Find the red blood cells and label each as P. falciparum-infected, uninfected, or of indeterminate infection status.
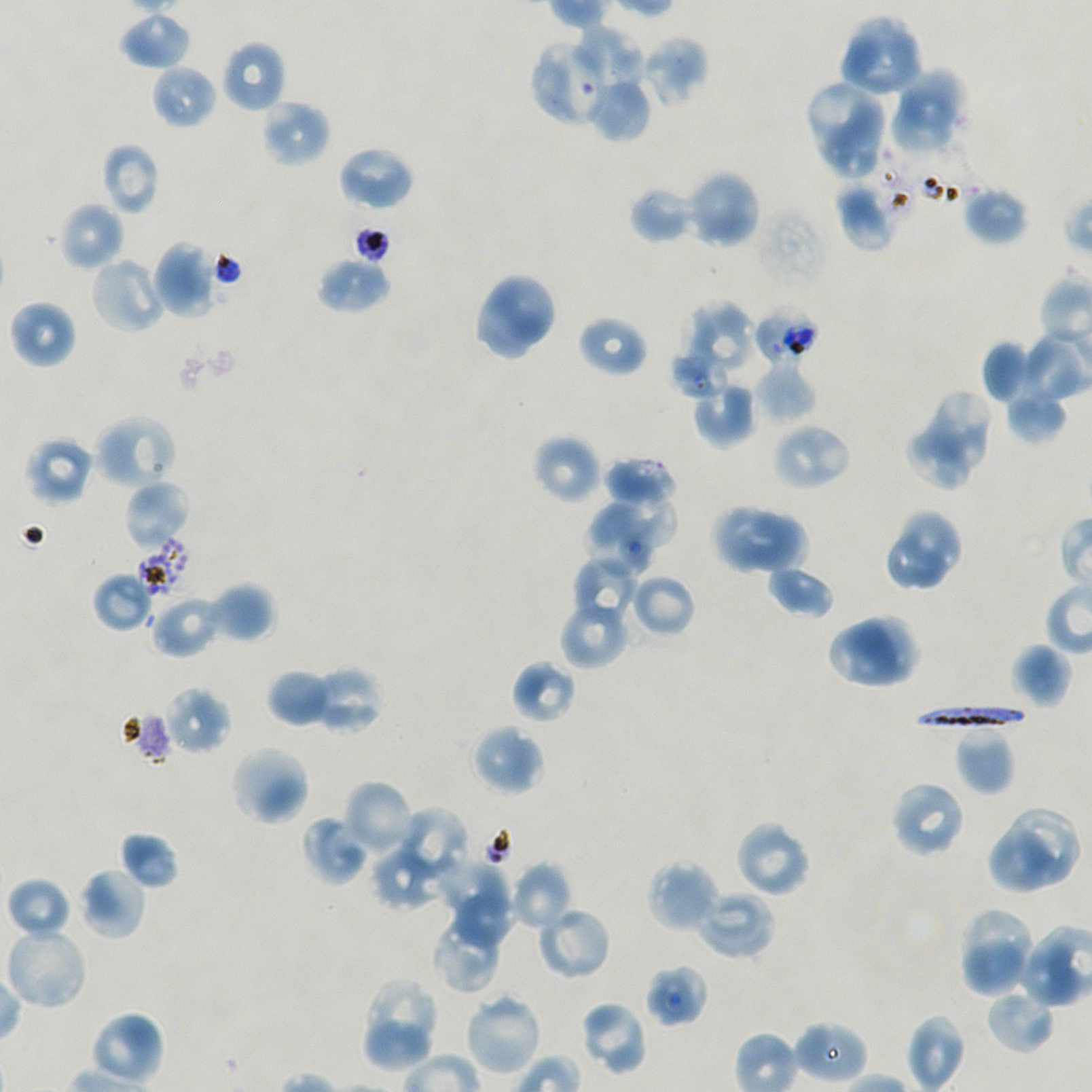

Approximate bounding boxes as {x1, y1, x2, y2} in pixels. Not every red blood cell is marked.
Infected red blood cells: {911, 704, 1032, 731}.
Red blood cells of indeterminate infection status: {530, 39, 609, 127}, {752, 306, 820, 367}, {670, 348, 728, 398}, {139, 537, 192, 596}, {122, 710, 172, 764}, {644, 964, 708, 1027}.
Uninfected red blood cells: {117, 11, 192, 71}, {838, 15, 924, 99}, {570, 26, 644, 101}, {640, 34, 708, 108}, {221, 40, 287, 113}, {151, 65, 218, 130}, {896, 69, 967, 128}, {586, 75, 651, 143}, {810, 79, 887, 147}, {261, 98, 331, 168}, {890, 107, 956, 153}, {818, 122, 879, 176}, {100, 142, 160, 215}, {336, 145, 415, 211}, {686, 169, 761, 249}, {835, 181, 898, 251}, {962, 185, 1030, 246}, {630, 186, 699, 244}, {56, 200, 125, 271}, {151, 240, 218, 318}, {88, 255, 168, 335}, {316, 256, 391, 314}, {484, 271, 558, 342}, {476, 290, 536, 361}, {8, 299, 77, 369}, {687, 301, 755, 372}, {577, 314, 649, 378}, {1017, 333, 1091, 405}, {981, 340, 1033, 404}, {752, 363, 816, 425}, {692, 380, 757, 447}, {1005, 388, 1068, 444}, {927, 390, 990, 471}, {92, 414, 177, 491}, {771, 422, 852, 492}, {907, 428, 972, 487}, {532, 434, 602, 504}, {24, 435, 95, 506}, {604, 456, 678, 507}, {124, 479, 191, 550}, {584, 491, 678, 570}, {710, 503, 782, 577}, {748, 508, 811, 580}, {899, 509, 964, 578}, {887, 534, 947, 592}, {572, 556, 642, 625}, {766, 564, 835, 618}, {92, 571, 155, 632}, {627, 572, 697, 639}, {205, 582, 275, 643}, {150, 594, 223, 658}, {558, 599, 630, 670}, {826, 612, 921, 689}, {1010, 642, 1073, 708}, {511, 660, 577, 726}, {308, 666, 382, 735}, {267, 668, 334, 727}, {164, 687, 231, 754}, {470, 724, 544, 796}, {955, 730, 1014, 796}, {228, 745, 310, 826}, {342, 780, 416, 856}, {890, 780, 968, 859}, {400, 806, 468, 877}, {1006, 809, 1082, 886}, {302, 816, 371, 886}, {733, 819, 812, 898}, {119, 831, 179, 889}, {987, 832, 1051, 894}, {373, 853, 439, 911}, {444, 858, 514, 920}, {647, 858, 721, 934}, {510, 863, 572, 930}, {77, 867, 148, 940}, {6, 877, 73, 941}, {695, 888, 776, 961}, {452, 896, 514, 946}, {536, 905, 612, 981}, {966, 909, 1033, 978}, {431, 911, 503, 994}, {3, 925, 90, 1011}, {958, 939, 1026, 998}, {1017, 939, 1078, 1008}, {359, 977, 439, 1073}, {985, 986, 1056, 1055}, {463, 991, 543, 1077}, {579, 1000, 649, 1076}, {88, 1009, 166, 1087}, {906, 1015, 966, 1092}, {794, 1021, 867, 1081}.

{
  "stain": "Giemsa",
  "culture": "in-vitro P. falciparum strain NF54, static",
  "donor_blood_group": "A+/O+",
  "field_of_view": "single",
  "preparation": "thin blood smear",
  "image_size": "1092×1092 pixels",
  "objective": "100x, oil immersion, numerical aperture 1.45"
}